Report the malaria status of this cell.
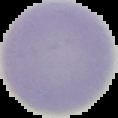
It is uninfected.

The area outside the segmented cell region is set to black. From a thin blood film. Image is 118×118 pixels.